Comment on the morphology of the erythrocytes.
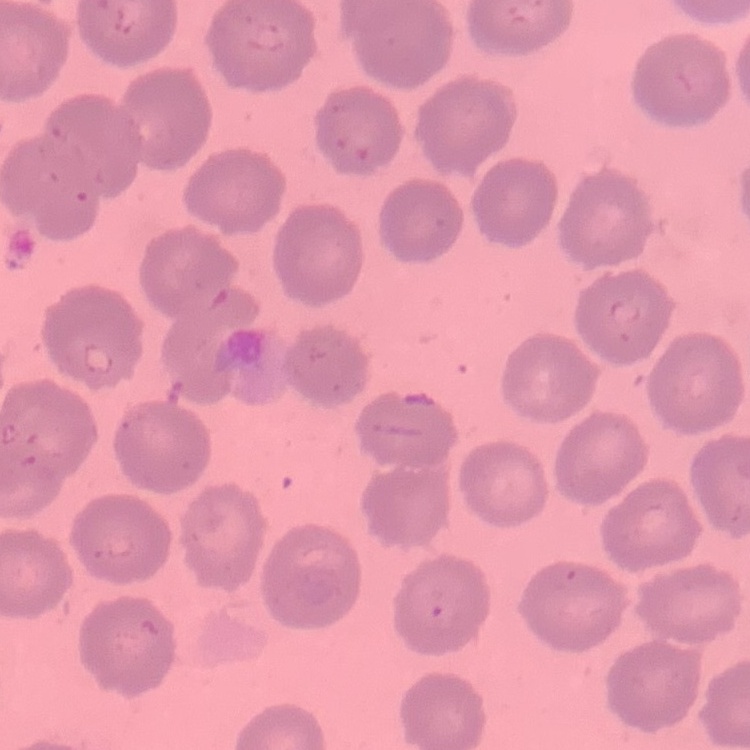

No rouleaux formation.

One tile cut from a larger photomicrograph. Field's or Giemsa stain. Thin blood film.